Assess the morphology of the erythrocytes.
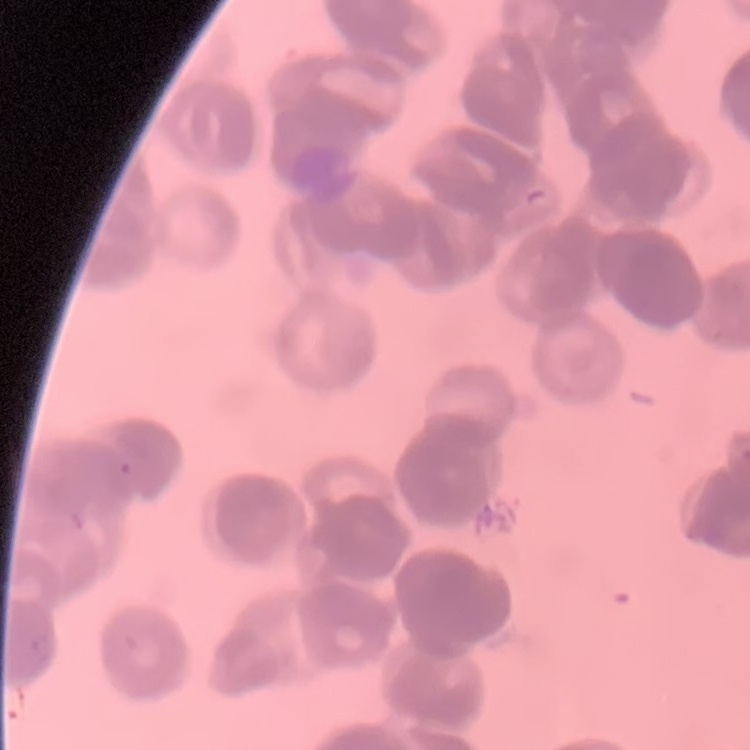
They show rouleaux formation.

stain = Field's or Giemsa
image type = square crop of a larger photomicrograph
preparation = thin peripheral smear